Assess the morphology of the erythrocytes.
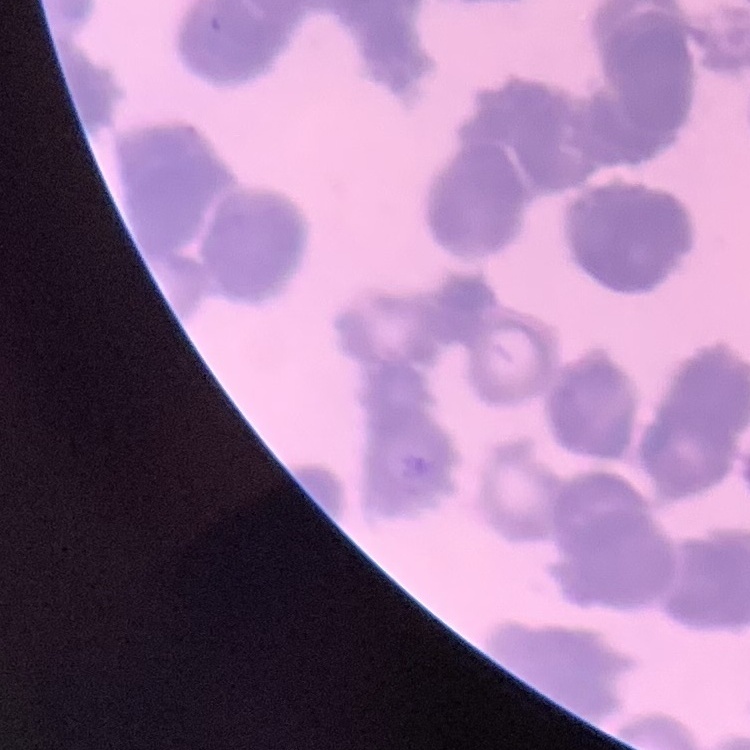
Rouleaux formation.

preparation = thin peripheral smear
image type = one tile cut from a larger photomicrograph
stain = Field's or Giemsa